Identify the parasite.
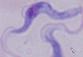

A trypanosome.

Summary:
  - Magnification: 1000x
  - Modality: micrograph